Describe the morphology of the erythrocytes.
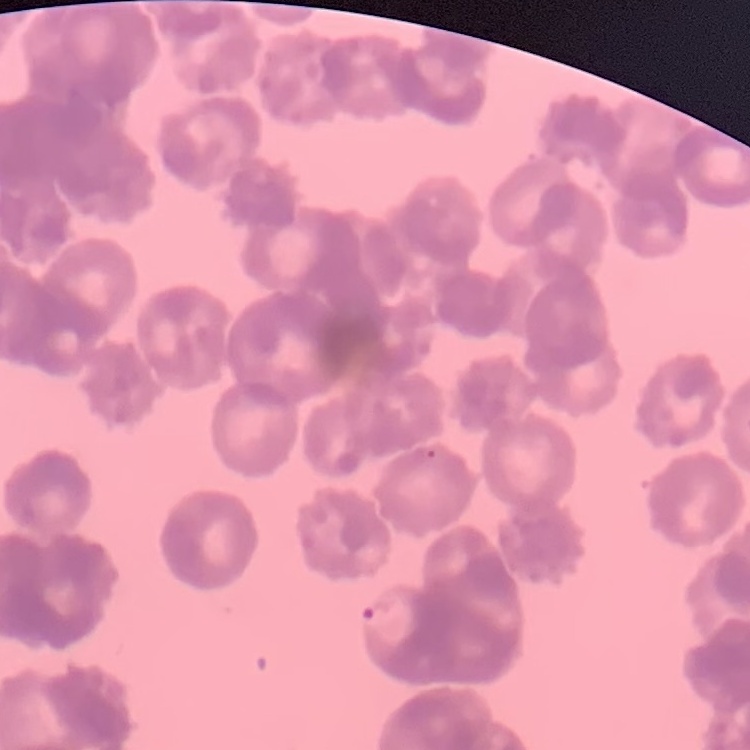
They show rouleaux formation.

image_type: square crop of a larger photomicrograph
preparation: thin blood film
stain: Field's or Giemsa